Report the malaria status of this cell.
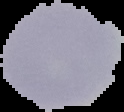
Uninfected.

image_type: cell region segmented out of the field of view; surrounding area masked to black
image_size: 124×112 pixels
preparation: thin blood smear